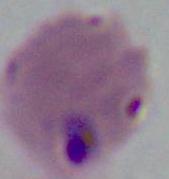

Micrograph. Captured at either 400x or 1000x magnification. A Plasmodium parasite is shown.